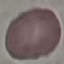

Malaria status: uninfected. Thin blood film. Giemsa-stained preparation. Automatically extracted cell patch, resized to 64 × 64 pixels. Acquired by smartphone through the microscope eyepiece.